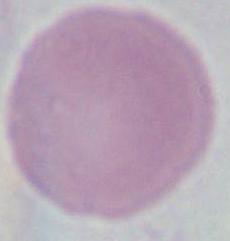
magnification = 1000x
modality = micrograph
identification = erythrocyte